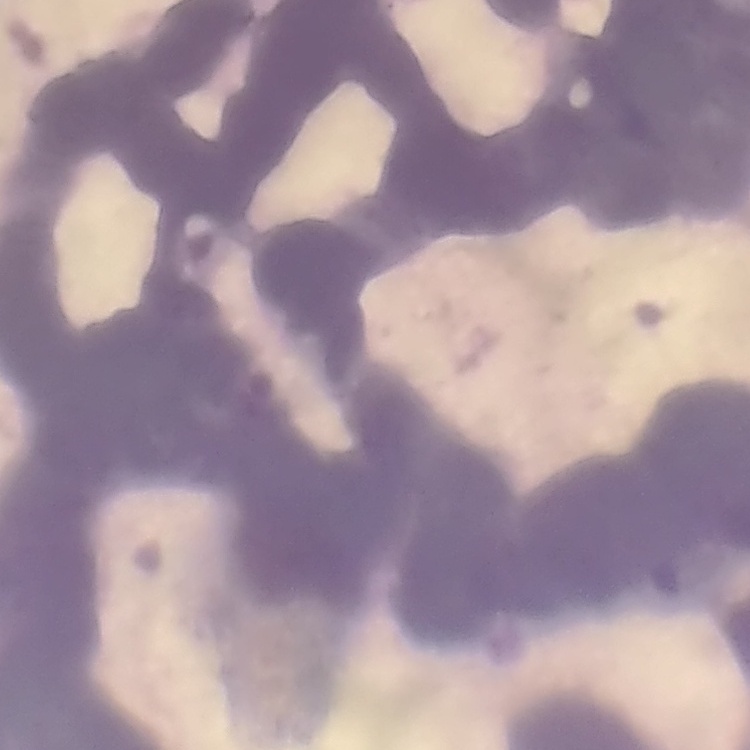

red blood cell morphology = rouleaux formation
image type = square crop of a larger photomicrograph
stain = Field's or Giemsa
preparation = thin blood smear